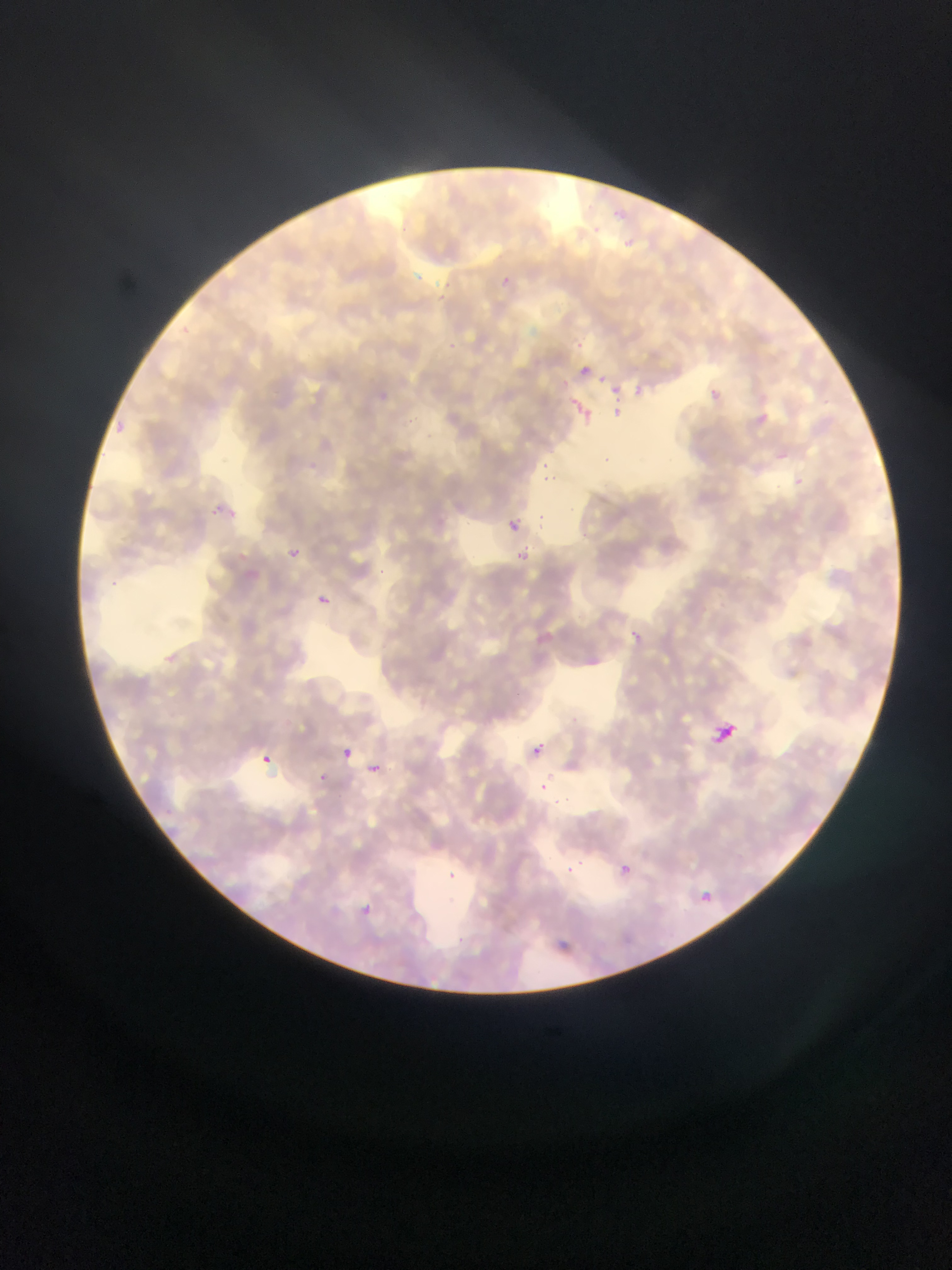

Approximate bounding boxes as [left, top, right, bottom] in pixels.
Summary:
  - Leukocyte locations: [708, 719, 739, 749]
  - Malaria parasite locations: [574, 361, 595, 381], [626, 382, 654, 405], [707, 386, 733, 404], [567, 397, 597, 427], [748, 405, 775, 423], [612, 407, 623, 421], [110, 422, 127, 430], [768, 450, 790, 466], [540, 457, 553, 465], [542, 467, 565, 490], [209, 504, 226, 520], [505, 516, 524, 536], [280, 542, 307, 566], [511, 547, 529, 564], [319, 588, 336, 606], [632, 626, 646, 643], [156, 647, 185, 672], [537, 734, 551, 749], [338, 745, 355, 762], [531, 746, 543, 761], [257, 753, 273, 767], [363, 759, 386, 780], [320, 773, 334, 787], [540, 777, 551, 789], [616, 861, 634, 878], [564, 864, 578, 876], [440, 870, 460, 884], [694, 890, 725, 913], [353, 900, 376, 922]
  - Country: Ghana
  - Capture: mobile-phone photograph through a microscope
  - Field of view: single
  - Image size: 952×1270 pixels
  - Preparation: thin blood smear